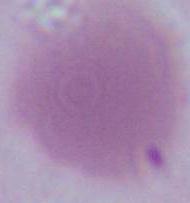

identification = erythrocyte
modality = micrograph
magnification = 1000x